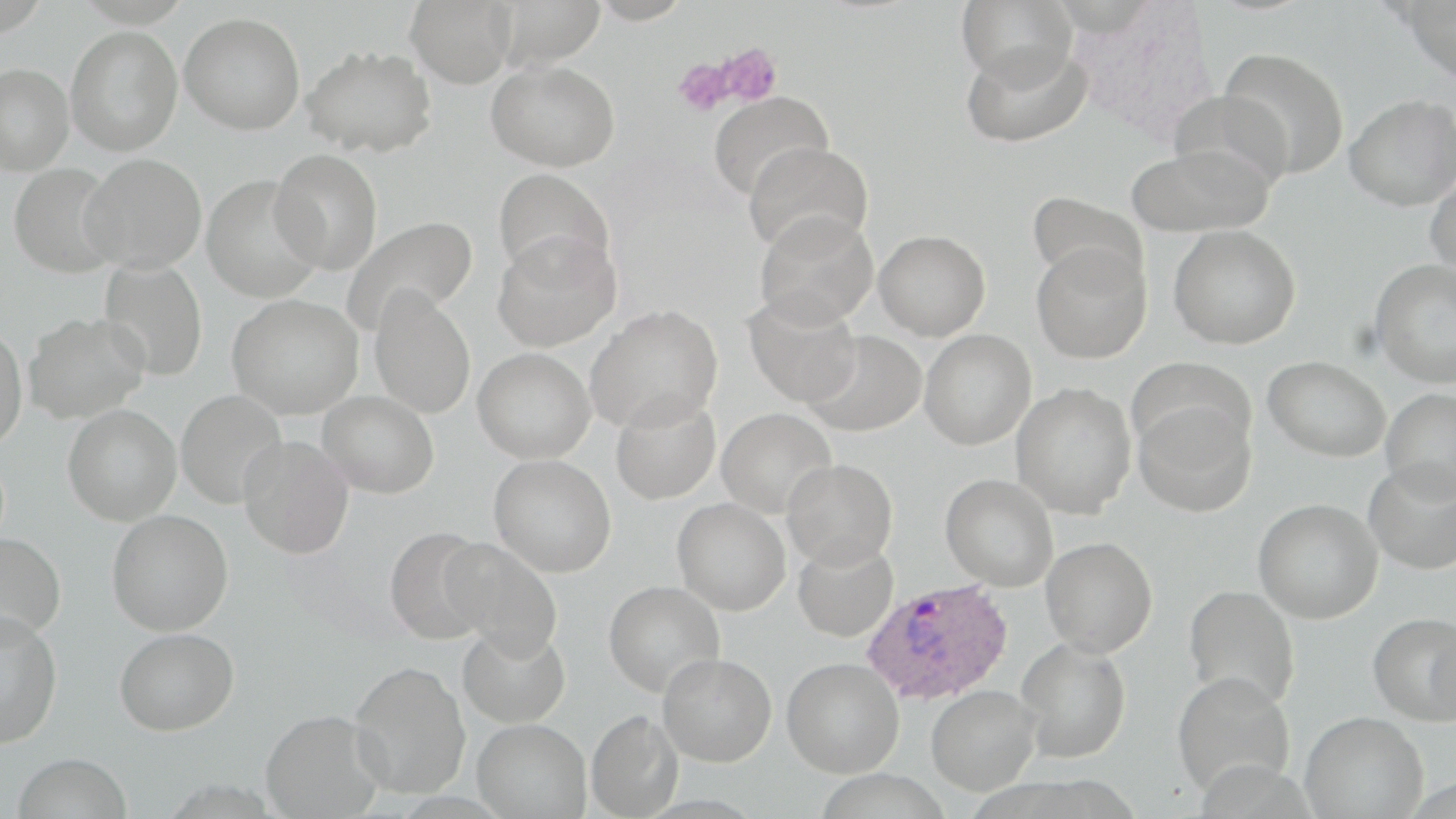
Approximate bounding boxes as (x1,y1)-(x2,y2) corner pairs in pixels. Plasmodium ovale-infected red blood cell locations: (860,577)-(1014,706). Uninfected red blood cell locations: (405,0)-(517,88), (492,0)-(607,68), (955,0)-(1077,91), (1401,1)-(1456,82), (179,12)-(305,135), (65,26)-(183,156), (960,41)-(1092,149), (301,45)-(438,158), (1218,47)-(1350,180), (487,59)-(620,172), (0,61)-(74,174), (1168,89)-(1294,195), (707,90)-(834,202), (1344,93)-(1456,210), (744,141)-(873,256), (1125,143)-(1274,237), (270,149)-(383,275), (80,153)-(207,273), (7,163)-(122,278), (493,166)-(616,283), (1425,168)-(1456,279), (202,175)-(325,303), (1027,191)-(1146,291), (754,209)-(878,329), (340,215)-(477,337), (1169,225)-(1301,349), (874,230)-(991,340), (492,233)-(622,352), (1031,241)-(1151,364), (1370,258)-(1456,388), (98,259)-(208,382), (369,288)-(476,419), (742,292)-(862,407), (227,294)-(364,419), (585,304)-(723,433), (24,311)-(150,423), (0,325)-(27,451), (919,329)-(1036,449), (803,331)-(926,437), (473,347)-(595,463), (1263,355)-(1390,462), (1129,358)-(1254,459), (1011,382)-(1137,518), (1380,387)-(1456,499), (175,390)-(287,509), (316,391)-(439,498), (610,393)-(721,506), (1133,399)-(1257,517), (62,405)-(182,525), (716,407)-(837,519), (237,435)-(354,558), (489,455)-(617,577), (781,458)-(898,569), (1363,460)-(1456,575), (940,473)-(1059,591), (672,498)-(791,615), (1253,498)-(1384,623), (106,510)-(233,635), (383,526)-(493,644), (0,533)-(66,642), (1041,536)-(1158,657), (441,538)-(563,659), (792,539)-(898,643), (603,580)-(725,698), (1184,584)-(1300,709), (0,610)-(63,749), (1368,612)-(1456,725), (457,622)-(572,729), (114,627)-(239,736), (1017,638)-(1131,763), (657,653)-(777,767), (782,656)-(904,777), (348,661)-(471,799), (1171,672)-(1296,796), (925,684)-(1040,796), (260,709)-(385,818), (586,710)-(682,818), (1300,711)-(1429,819), (472,718)-(591,818), (11,753)-(134,819). Platelet locations: (709,43)-(784,108), (672,56)-(735,117). Slide-level diagnosis: Plasmodium ovale. May-Grünwald-Giemsa-stained preparation. Optical microscopy. Captured at 1000x magnification. Image is 1456×819 pixels. Thin blood film. Single field of view.